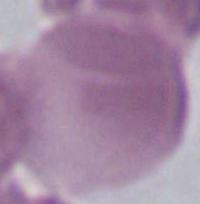

magnification = 1000x
modality = photomicrograph
identification = red blood cell